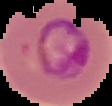

malaria status = parasitized
preparation = thin blood smear
image type = segmented cell region with the area outside set to black
image size = 112×106 pixels